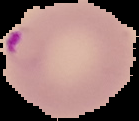

Summary:
  - Image size: 139×121 pixels
  - Image type: segmented cell region on a black background
  - Result: Plasmodium parasites detected
  - Preparation: thin blood smear